Report the malaria status of this cell.
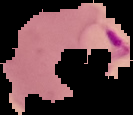
Parasitized.

preparation = thin blood film
image type = segmented cell region with the area outside set to black
image size = 133×115 pixels